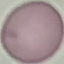
result = no malaria parasites detected
image type = cell patch, automatically extracted from a larger field of view and resized to 64 × 64 pixels
capture = smartphone camera at the microscope eyepiece
stain = Giemsa
preparation = thin blood smear